Point out each leukocyte.
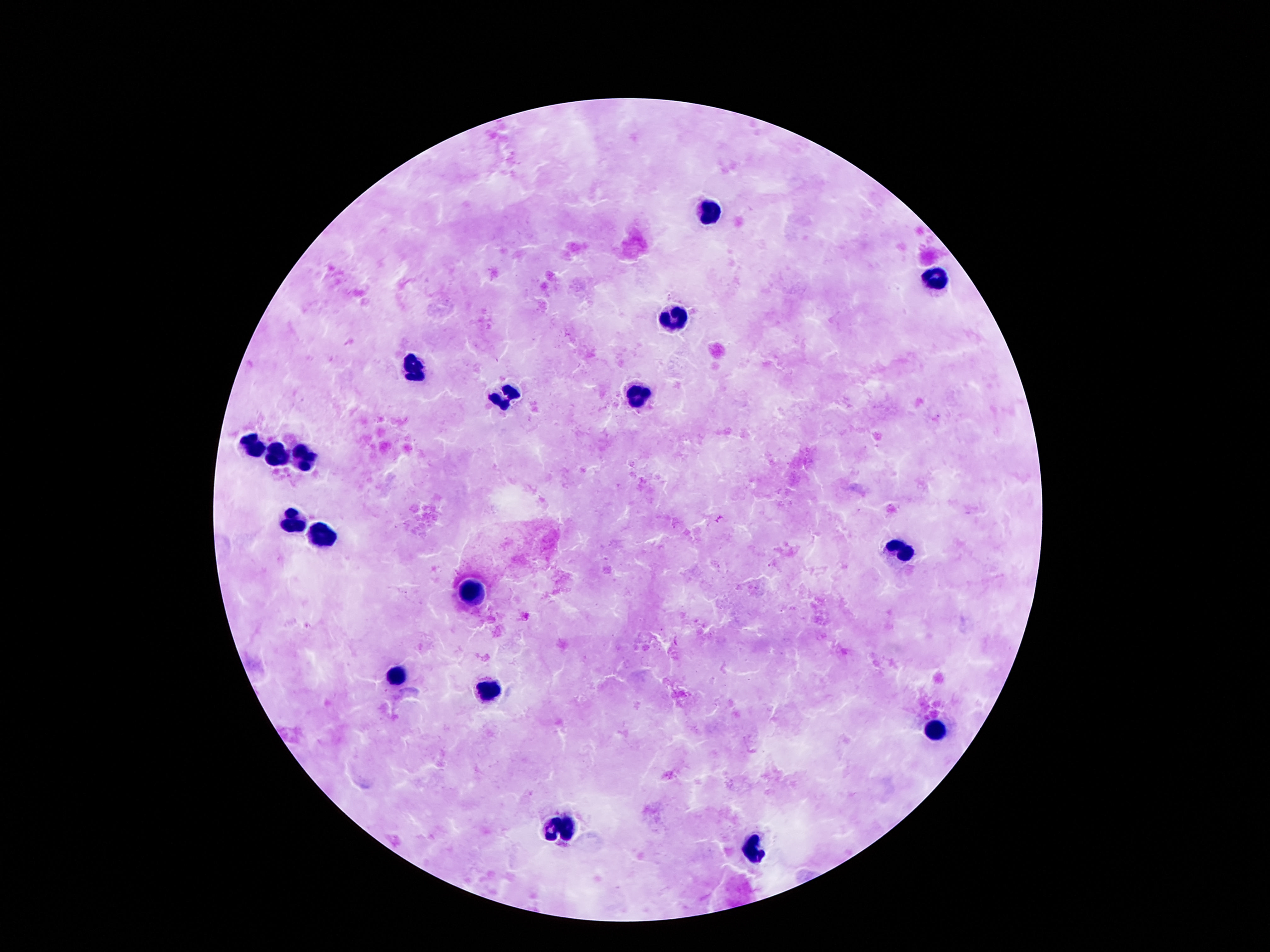

Approximate object centers, in pixels from the top-left corner.
Leukocytes: (x=712, y=213), (x=937, y=279), (x=673, y=315), (x=413, y=365), (x=505, y=395), (x=636, y=395), (x=253, y=445), (x=305, y=456), (x=276, y=457), (x=292, y=518), (x=321, y=536), (x=902, y=555), (x=470, y=592), (x=397, y=678), (x=487, y=689), (x=935, y=734), (x=563, y=826), (x=755, y=847).

Patient malaria status: uninfected. Single field of view. 100x magnification. Image is 1270×952 pixels. Smartphone photograph taken through the microscope eyepiece. Giemsa-stained preparation. Thick peripheral-blood smear.